Report the malaria status of this cell.
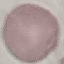
Uninfected.

Thin blood film. Acquired by smartphone through the microscope eyepiece. Automatically extracted cell patch, resized to 64 × 64 pixels. Giemsa-stained preparation.